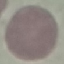
Summary:
  - Result: no malaria parasites seen
  - Image type: cell patch, automatically extracted from a larger field of view and resized to 64 × 64 pixels
  - Preparation: thin blood smear
  - Capture: smartphone camera at the microscope eyepiece
  - Stain: Giemsa